Evaluate for Plasmodium parasites.
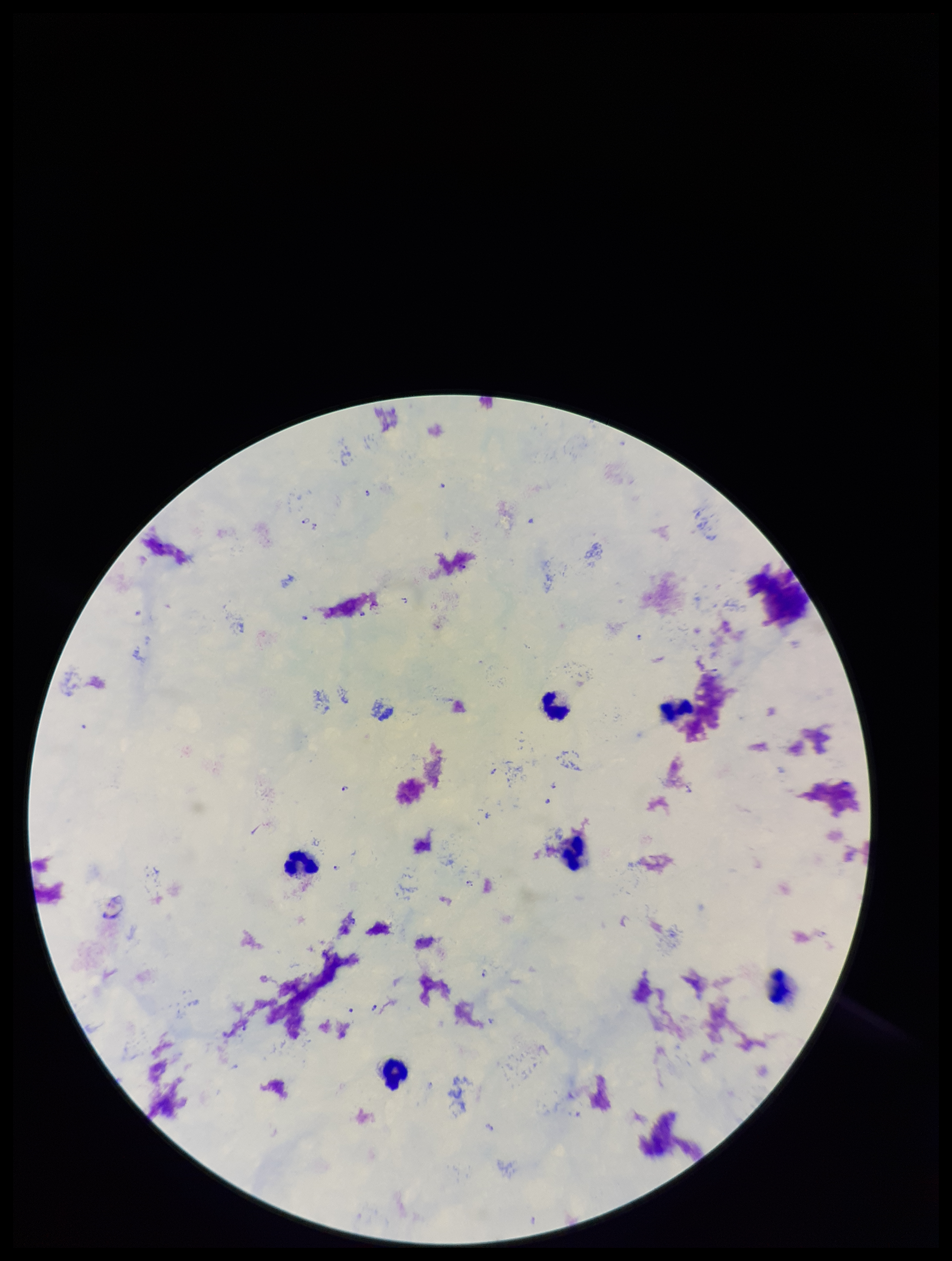
Detected.

Parasite count: 12. Stained with Giemsa. Patient malaria status: positive. Image is 952×1261 pixels. Preparation: thick blood smear. Leukocyte count: 6. One field from this slide. Photographed through the microscope eyepiece with a smartphone camera. Species reported for this patient: Plasmodium falciparum.